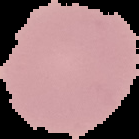

Summary:
  - Malaria status: uninfected
  - Preparation: thin blood film
  - Image type: segmented cell region with the area outside set to black
  - Image size: 139×139 pixels